Identify the parasite.
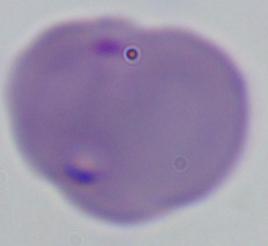

Babesia.

magnification = 1000x
modality = photomicrograph